Name the parasite shown.
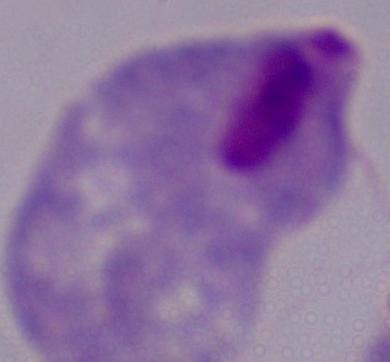
This is a trichomonad.

modality: photomicrograph
magnification: 1000x